Name the parasite shown.
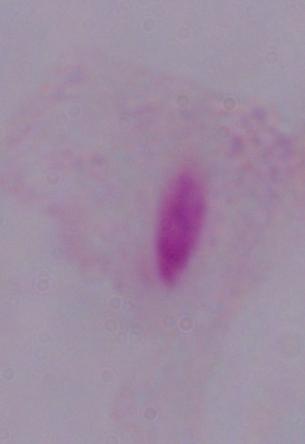
A trichomonad.

Summary:
  - Magnification: 1000x
  - Modality: micrograph